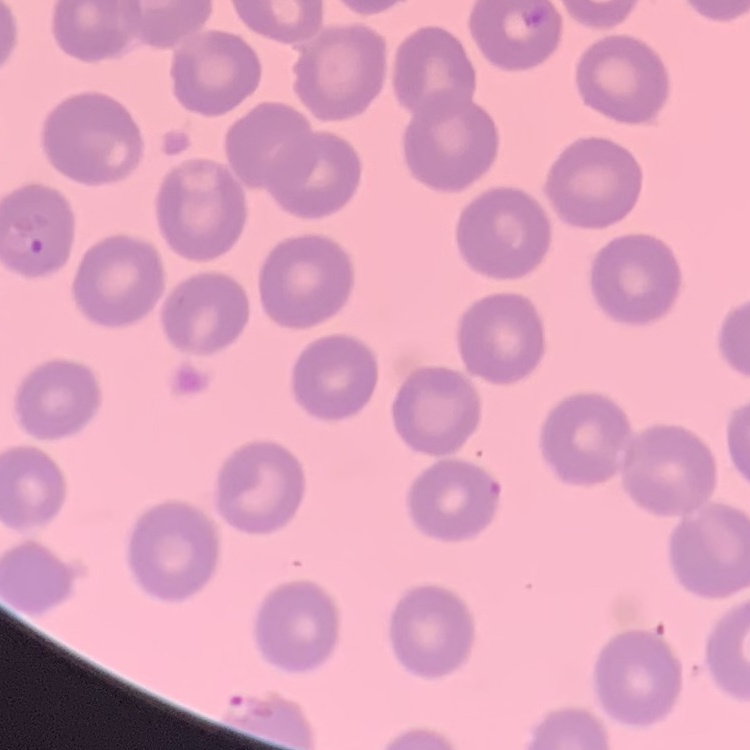

erythrocyte morphology = no rouleaux formation
stain = Field's or Giemsa
preparation = thin peripheral smear
image type = square crop of a larger photomicrograph